Name the blood parasite species.
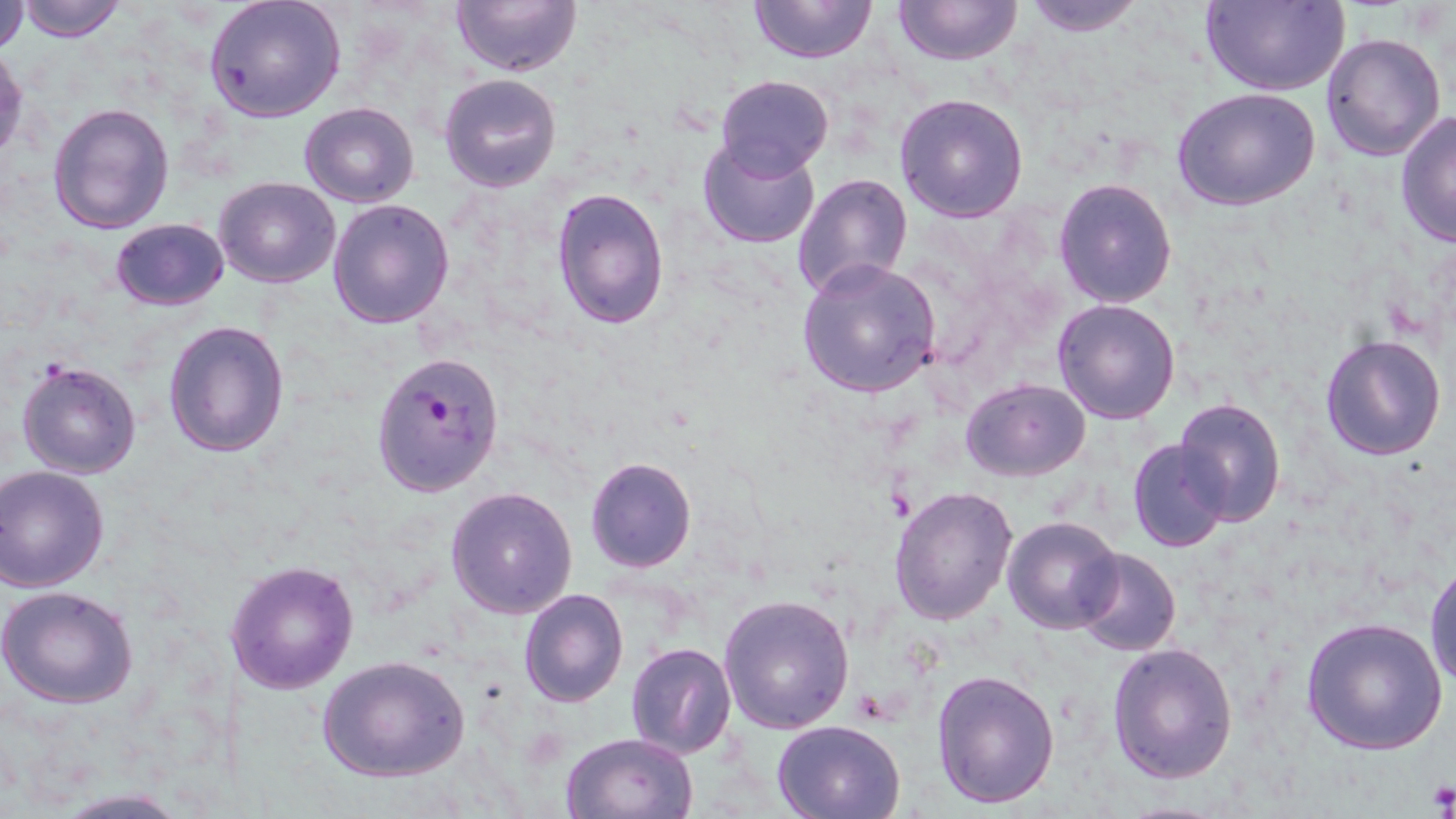

Plasmodium falciparum.

stain: May-Grünwald-Giemsa
plasmodium_falciparum_infected_red_blood_cell_locations: 'approximate bounding boxes as [x1, y1, x2, y2] in pixels: [371, 349, 504, 498]'
uninfected_red_blood_cell_locations: 'approximate bounding boxes as [x1, y1, x2, y2] in pixels: [13, 0, 129, 41], [204, 0, 347, 123], [451, 0, 583, 76], [748, 0, 877, 65], [892, 0, 1023, 67], [1018, 0, 1150, 35], [1200, 1, 1350, 96], [0, 3, 30, 53], [1320, 31, 1446, 162], [1, 47, 26, 164], [438, 73, 562, 192], [716, 74, 833, 177], [1174, 88, 1319, 211], [894, 92, 1029, 223], [47, 101, 174, 234], [299, 103, 419, 207], [1396, 109, 1456, 250], [697, 135, 822, 250], [792, 172, 913, 300], [214, 177, 340, 288], [1053, 179, 1177, 307], [552, 186, 669, 330], [328, 198, 455, 329], [109, 218, 228, 310], [796, 257, 942, 398], [1052, 299, 1181, 425], [162, 319, 289, 456], [1319, 333, 1447, 462], [15, 359, 143, 480], [961, 379, 1091, 480], [1172, 397, 1287, 525], [1127, 439, 1231, 552], [585, 457, 697, 573], [2, 464, 111, 591], [445, 484, 578, 618], [890, 485, 1018, 625], [1003, 517, 1123, 634], [1072, 547, 1180, 657], [225, 559, 359, 693], [1426, 563, 1456, 695], [0, 586, 139, 710], [519, 589, 629, 708], [719, 593, 854, 735], [1300, 617, 1448, 757], [625, 642, 738, 760], [1107, 642, 1238, 783], [317, 654, 470, 783], [931, 669, 1060, 810], [772, 719, 906, 818], [562, 733, 699, 819]'
preparation: thin blood smear
platelet_locations: 'approximate bounding boxes as [x1, y1, x2, y2] in pixels: [1426, 780, 1456, 815]'
magnification: 1000x
image_size: 1456×819 pixels
modality: optical microscopy
field_of_view: one of a larger specimen